Locate every blood parasite and identify its species.
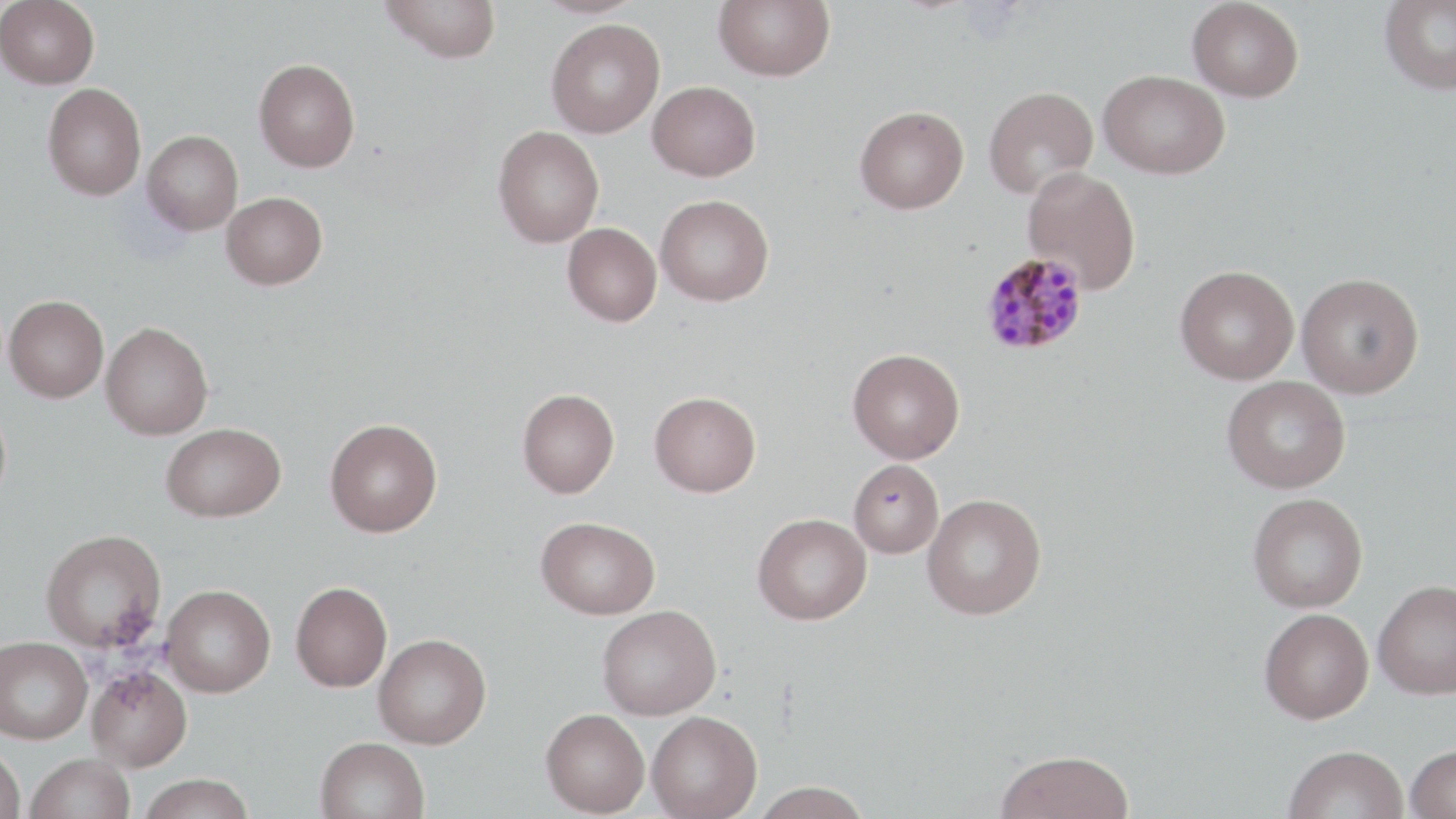
Approximate bounding boxes as (x1,y1)-(x2,y2) corner pairs in pixels.
Plasmodium malariae-infected red blood cells: (980,251)-(1089,356).
No Plasmodium falciparum, Plasmodium ovale, Plasmodium vivax, Babesia divergens, or Trypanosoma brucei observed.

Summary:
  - Uninfected red blood cell locations: (0,0)-(100,89), (381,0)-(502,63), (714,0)-(835,81), (1187,0)-(1304,102), (1379,0)-(1456,95), (546,19)-(665,138), (253,58)-(360,172), (1098,70)-(1230,179), (647,81)-(761,181), (42,83)-(146,200), (983,85)-(1098,199), (854,105)-(969,214), (493,126)-(604,247), (142,130)-(243,235), (1022,167)-(1141,294), (221,191)-(327,289), (655,194)-(774,306), (563,222)-(662,326), (1175,265)-(1299,385), (1297,272)-(1424,398), (4,295)-(108,402), (101,321)-(213,440), (847,348)-(965,463), (1221,376)-(1351,493), (517,388)-(619,498), (649,391)-(761,496), (0,403)-(11,510), (325,419)-(443,537), (161,422)-(286,522), (848,459)-(944,558), (1247,492)-(1368,612), (921,493)-(1046,619), (753,513)-(871,625), (536,516)-(660,619), (40,529)-(166,652), (1373,579)-(1456,698), (290,580)-(392,691), (161,584)-(276,697), (597,605)-(721,720), (1259,608)-(1373,724), (373,633)-(491,749), (0,636)-(92,744), (87,665)-(193,771), (541,708)-(650,816), (647,710)-(762,819), (316,736)-(430,819), (1284,744)-(1409,819), (1406,744)-(1456,818), (0,747)-(26,819), (996,749)-(1134,819), (25,753)-(135,819), (138,774)-(256,818), (750,781)-(875,818)
  - Slide-level diagnosis: Plasmodium malariae
  - Modality: optical microscopy
  - Stain: May-Grünwald-Giemsa
  - Preparation: thin blood smear
  - Image size: 1456×819 pixels
  - Magnification: 1000x
  - Field of view: single